State the blood parasite species.
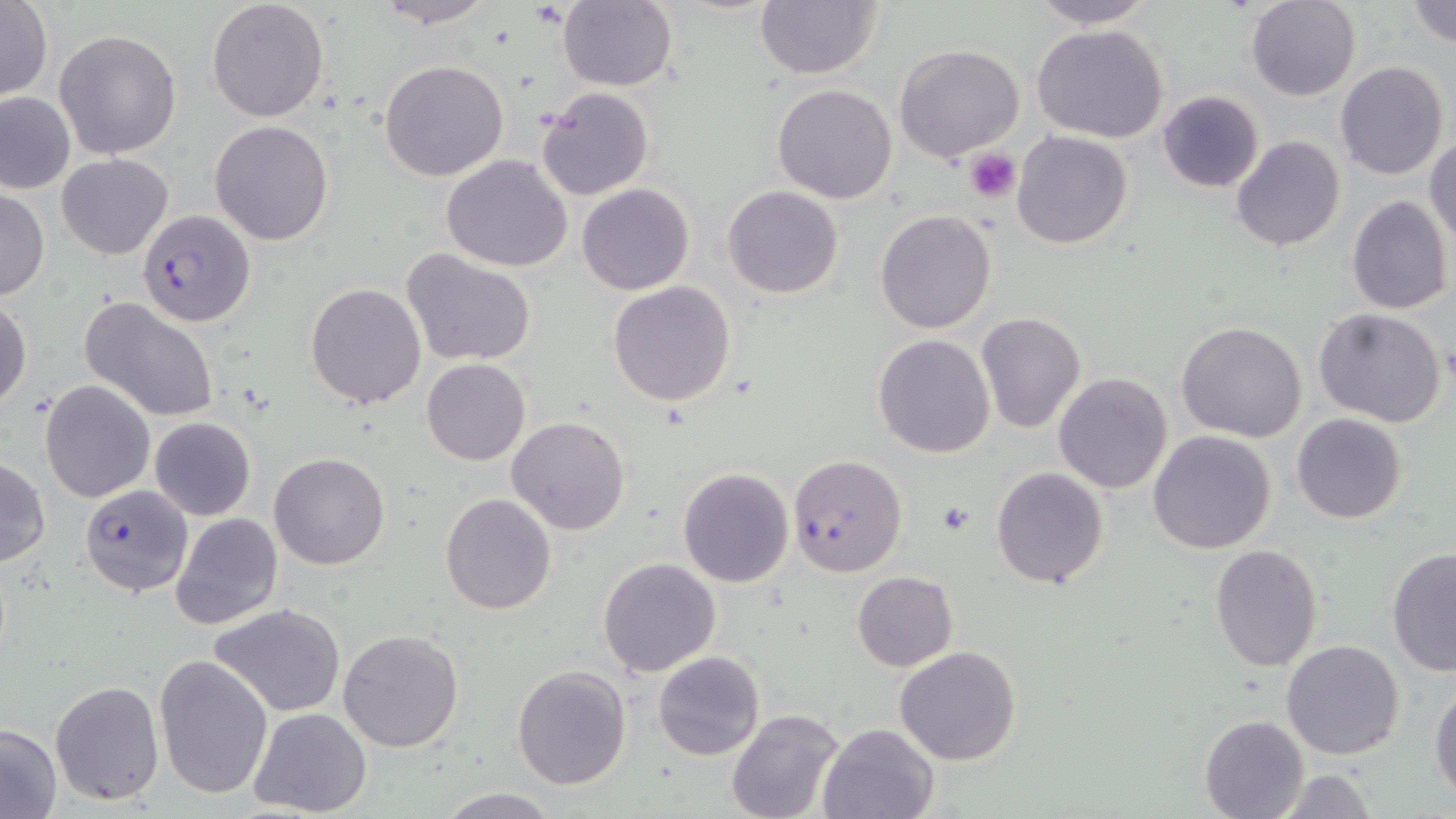
Plasmodium falciparum.

uninfected_red_blood_cell_locations: 'approximate bounding boxes as (x1,y1)-(x2,y2) corner pairs in pixels: (206,0)-(330,121), (372,0)-(496,29), (1026,0)-(1156,29), (1245,0)-(1362,102), (1407,0)-(1456,47), (0,1)-(52,102), (556,1)-(677,90), (754,1)-(883,80), (1030,25)-(1172,144), (54,29)-(182,159), (894,44)-(1025,164), (379,60)-(510,182), (1335,61)-(1449,182), (771,84)-(898,204), (537,86)-(653,200), (0,89)-(75,194), (1158,90)-(1265,192), (210,120)-(332,246), (1012,131)-(1133,248), (1427,133)-(1456,250), (1229,135)-(1346,254), (56,153)-(174,259), (442,155)-(574,271), (577,183)-(694,295), (722,185)-(846,298), (0,189)-(49,301), (1345,195)-(1453,315), (874,210)-(997,334), (401,249)-(538,368), (609,281)-(737,406), (305,282)-(426,407), (79,296)-(221,423), (0,298)-(32,411), (1312,307)-(1449,427), (975,312)-(1086,435), (1176,321)-(1309,442), (872,334)-(996,457), (422,358)-(530,467), (1053,372)-(1175,493), (40,381)-(156,503), (1292,413)-(1407,524), (149,416)-(256,521), (506,417)-(631,535), (1148,430)-(1276,554), (269,453)-(390,571), (0,455)-(50,568), (678,466)-(794,586), (991,467)-(1109,588), (440,493)-(557,614), (169,511)-(283,629), (1210,543)-(1323,671), (1385,548)-(1456,676), (598,556)-(721,677), (852,571)-(957,671), (209,604)-(347,717), (338,629)-(465,753), (1281,639)-(1405,759), (894,646)-(1023,767), (653,650)-(765,760), (152,654)-(274,800), (510,664)-(633,790), (49,679)-(164,805), (1429,683)-(1455,801), (248,707)-(373,818), (726,709)-(845,819), (1198,714)-(1308,819), (818,721)-(941,818), (0,724)-(62,816), (1270,767)-(1379,819), (433,788)-(566,818)'
plasmodium_falciparum_infected_red_blood_cell_locations: 'approximate bounding boxes as (x1,y1)-(x2,y2) corner pairs in pixels: (137,210)-(256,327), (787,454)-(908,576), (79,483)-(192,597)'
modality: optical microscopy
stain: May-Grünwald-Giemsa
field_of_view: one of a larger specimen
platelet_locations: 'approximate bounding boxes as (x1,y1)-(x2,y2) corner pairs in pixels: (963,149)-(1022,203), (934,501)-(976,538)'
preparation: thin blood smear
magnification: 1000x
image_size: 1456×819 pixels